Assess this cell for malaria.
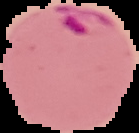

It is parasitized.

Summary:
  - Image size: 139×133 pixels
  - Image type: segmented cell region with the area outside set to black
  - Preparation: thin blood film